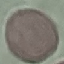

Malaria status: uninfected. Giemsa stain. Automatically extracted cell patch, resized to 64 × 64 pixels. Photographed with a smartphone camera at the microscope eyepiece. Thin blood film.